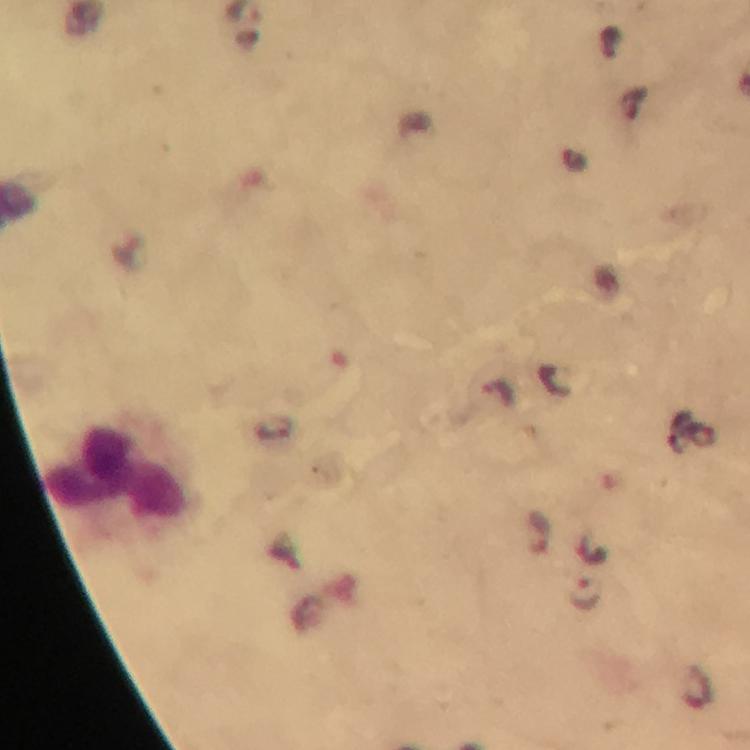
Approximate centers as (x, y) in pixels.
Summary:
  - Leukocyte locations: (117, 480)
  - Plasmodium parasite locations: (538, 532), (584, 595)
  - Stain: Giemsa
  - Cropped from: a single field of view
  - Capture: smartphone mounted on the microscope
  - Immersion oil: applied
  - Context: from a malaria diagnostic workup
  - Preparation: thick smear
  - Magnification: 100x
  - Image size: 750×750 pixels